State which cell type is depicted.
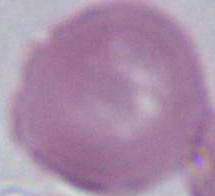

This is an erythrocyte.

{
  "magnification": "1000x",
  "modality": "photomicrograph"
}